Assess this cell for malaria.
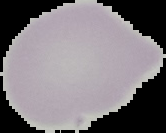
Uninfected.

Image is 166×133 pixels. Segmented cell region on a black background. From a thin blood smear.